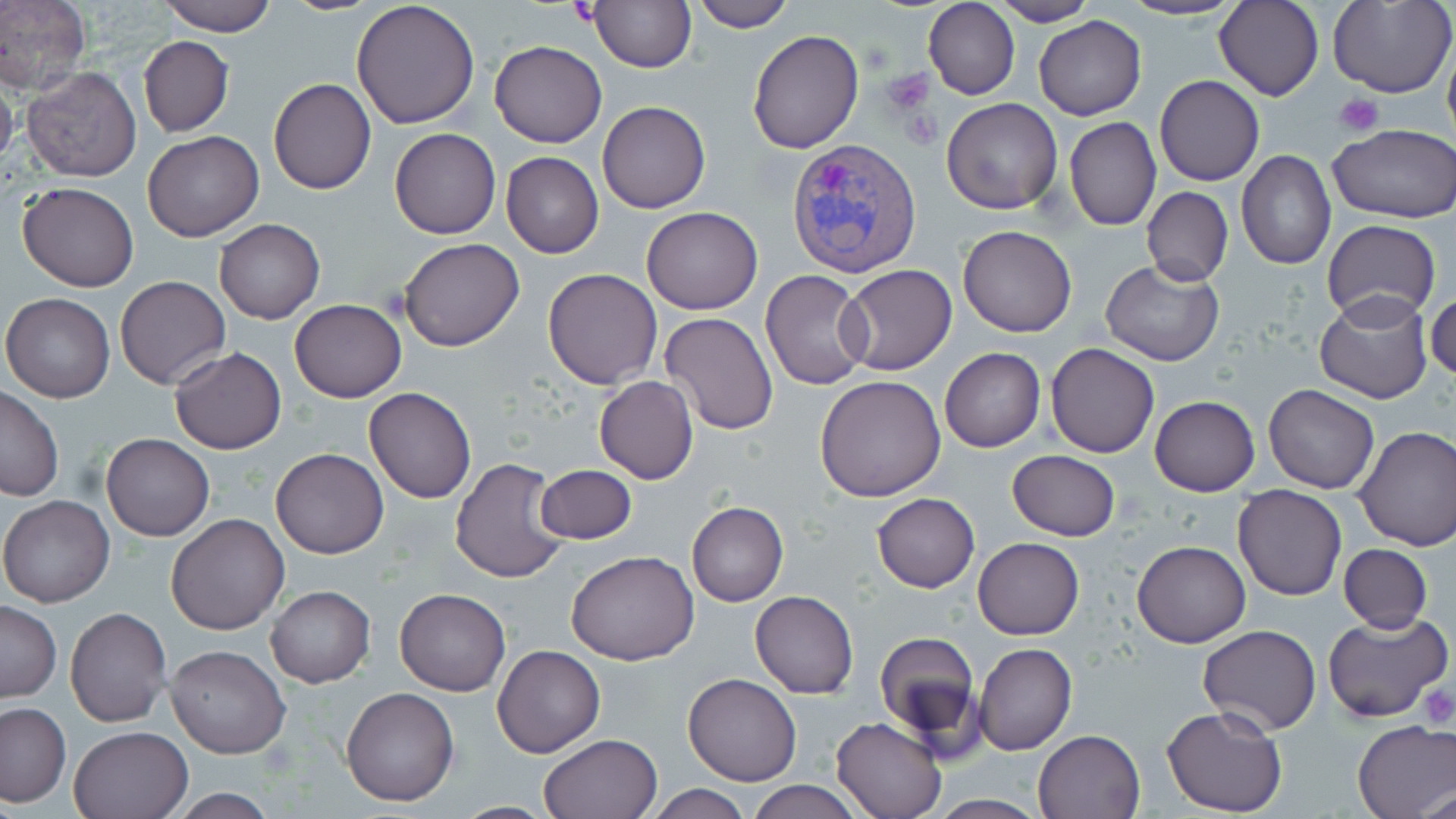

Summary:
  - Coordinate format: approximate bounding boxes as (x1,y1)-(x2,y2) corner pairs in pixels
  - Plasmodium vivax-infected red blood cell locations: (786,139)-(922,281)
  - Platelet locations: (883,68)-(933,113), (1334,94)-(1384,137), (1419,685)-(1455,727)
  - Uninfected red blood cell locations: (0,0)-(91,96), (158,0)-(276,35), (588,0)-(696,72), (684,0)-(796,32), (1115,0)-(1245,22), (1214,0)-(1324,102), (1329,0)-(1455,99), (351,1)-(482,131), (988,1)-(1097,25), (923,2)-(1019,100), (1033,15)-(1146,120), (747,29)-(864,153), (139,35)-(233,137), (1442,39)-(1456,154), (489,40)-(607,148), (21,65)-(143,183), (0,68)-(18,175), (1154,75)-(1264,185), (268,78)-(377,195), (942,98)-(1063,214), (597,101)-(711,214), (1064,116)-(1161,231), (1328,124)-(1456,222), (389,128)-(500,239), (143,130)-(263,241), (501,151)-(604,257), (1237,151)-(1335,271), (18,181)-(140,292), (1141,186)-(1233,286), (640,206)-(763,313), (214,219)-(324,323), (1321,219)-(1441,325), (958,224)-(1077,338), (399,238)-(525,352), (1100,261)-(1224,367), (839,264)-(956,376), (542,267)-(664,389), (760,271)-(874,390), (115,275)-(231,389), (1313,289)-(1434,405), (1426,290)-(1456,381), (2,293)-(116,403), (289,298)-(406,402), (659,312)-(779,435), (1046,342)-(1158,458), (170,347)-(286,454), (939,347)-(1045,452), (814,374)-(948,503), (594,375)-(699,484), (1264,384)-(1379,493), (0,386)-(64,502), (364,387)-(477,503), (1150,395)-(1259,495), (1354,425)-(1456,551), (101,433)-(214,542), (271,448)-(387,559), (1007,450)-(1120,540), (450,457)-(568,584), (536,464)-(637,545), (1232,484)-(1347,601), (871,492)-(980,593), (0,495)-(114,608), (687,501)-(788,607), (166,513)-(289,636), (972,537)-(1084,639), (1132,540)-(1251,649), (1339,544)-(1432,633), (567,549)-(699,665), (265,585)-(374,688), (394,587)-(511,696), (750,589)-(858,697), (1,602)-(61,702), (65,607)-(173,728), (1323,609)-(1452,724), (1196,624)-(1322,734), (874,631)-(983,752), (973,643)-(1077,757), (493,644)-(605,757), (165,645)-(290,759), (684,674)-(801,786), (340,686)-(459,806), (0,703)-(71,806), (1160,704)-(1289,817), (831,717)-(945,819), (1352,719)-(1456,819), (69,727)-(192,818), (1033,730)-(1145,818), (539,733)-(662,818), (747,780)-(866,818), (644,784)-(754,819), (1417,786)-(1456,819), (166,787)-(279,818), (925,796)-(1051,818)
  - Slide-level diagnosis: Plasmodium vivax
  - Stain: May-Grünwald-Giemsa
  - Image size: 1456×819 pixels
  - Magnification: 1000x
  - Preparation: thin blood smear
  - Field of view: single
  - Modality: optical microscopy